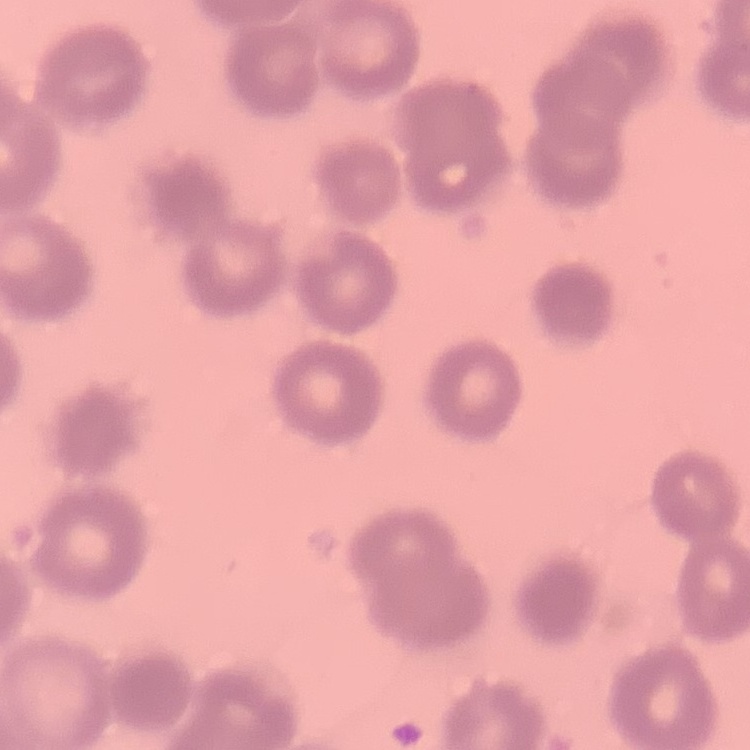 The red blood cells exhibit rouleaux formation. Field's or Giemsa stain. Square crop of a larger photomicrograph. Thin blood smear.